Identify the blood parasite species.
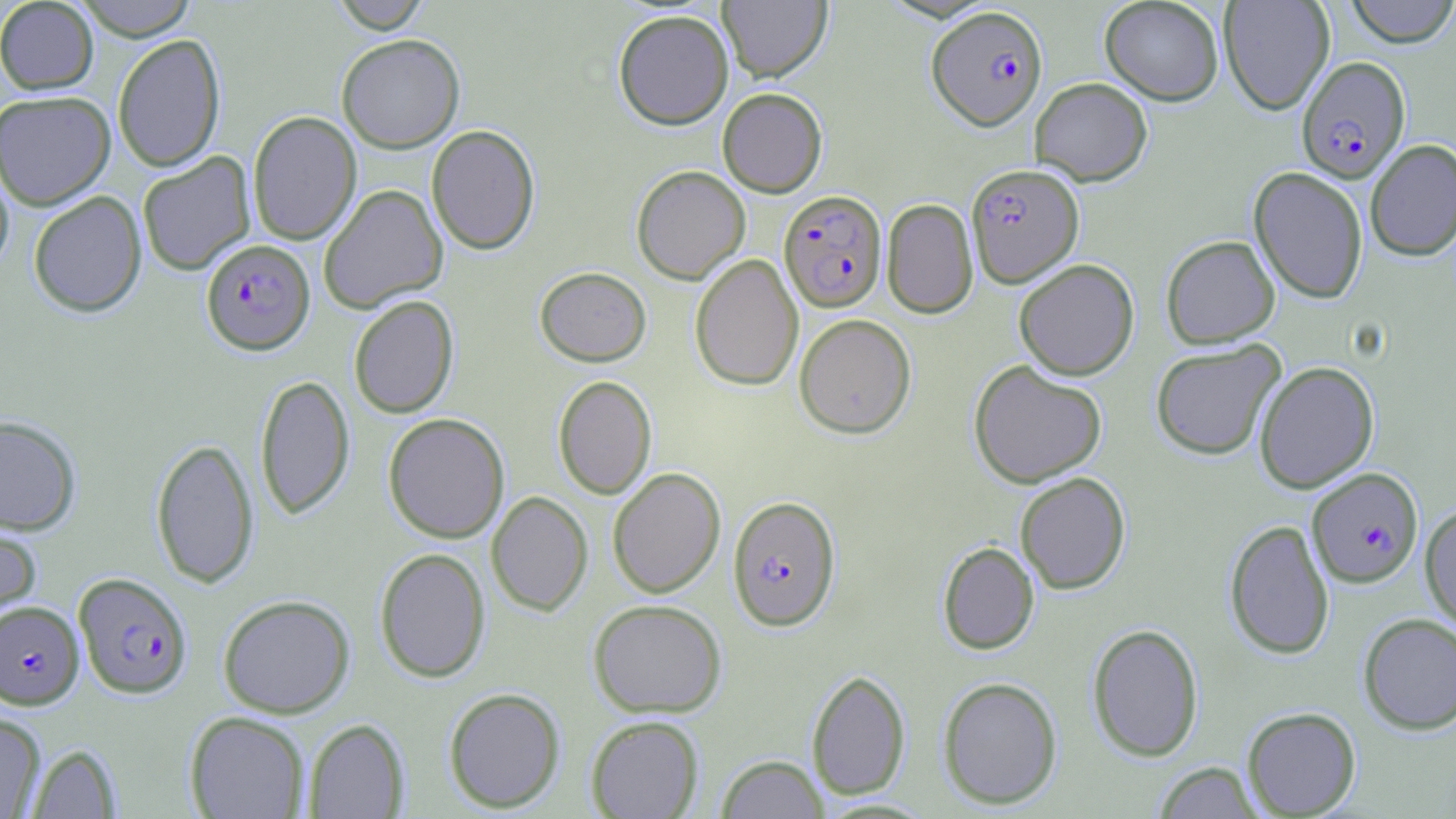

Plasmodium falciparum.

Summary:
  - Coordinate format: approximate bounding boxes as named x1/y1/x2/y2 corners in pixels
  - Plasmodium falciparum-infected red blood cell locations: (x1=927, y1=5, x2=1048, y2=130), (x1=1297, y1=56, x2=1411, y2=183), (x1=966, y1=163, x2=1084, y2=286), (x1=779, y1=189, x2=887, y2=312), (x1=201, y1=238, x2=315, y2=355), (x1=1307, y1=467, x2=1423, y2=587), (x1=727, y1=495, x2=841, y2=631), (x1=73, y1=572, x2=193, y2=698), (x1=1, y1=601, x2=84, y2=709)
  - Uninfected red blood cell locations: (x1=0, y1=0, x2=99, y2=94), (x1=72, y1=0, x2=198, y2=40), (x1=329, y1=0, x2=433, y2=33), (x1=718, y1=0, x2=832, y2=82), (x1=1099, y1=0, x2=1224, y2=105), (x1=1219, y1=0, x2=1334, y2=115), (x1=1343, y1=0, x2=1456, y2=47), (x1=613, y1=9, x2=733, y2=130), (x1=336, y1=33, x2=465, y2=153), (x1=112, y1=34, x2=226, y2=172), (x1=1029, y1=77, x2=1153, y2=186), (x1=717, y1=87, x2=827, y2=197), (x1=0, y1=90, x2=116, y2=209), (x1=247, y1=111, x2=362, y2=245), (x1=426, y1=124, x2=541, y2=255), (x1=1365, y1=139, x2=1456, y2=261), (x1=137, y1=152, x2=256, y2=276), (x1=0, y1=158, x2=14, y2=277), (x1=631, y1=165, x2=750, y2=284), (x1=1248, y1=166, x2=1368, y2=304), (x1=318, y1=184, x2=448, y2=313), (x1=28, y1=190, x2=147, y2=317), (x1=881, y1=199, x2=978, y2=318), (x1=1160, y1=235, x2=1280, y2=348), (x1=689, y1=254, x2=803, y2=391), (x1=1014, y1=259, x2=1139, y2=380), (x1=535, y1=266, x2=651, y2=366), (x1=348, y1=295, x2=459, y2=419), (x1=794, y1=313, x2=916, y2=438), (x1=1150, y1=340, x2=1286, y2=460), (x1=969, y1=360, x2=1107, y2=488), (x1=1254, y1=361, x2=1379, y2=493), (x1=254, y1=373, x2=355, y2=520), (x1=552, y1=375, x2=657, y2=500), (x1=383, y1=413, x2=510, y2=543), (x1=0, y1=414, x2=82, y2=535), (x1=150, y1=437, x2=259, y2=588), (x1=607, y1=467, x2=726, y2=598), (x1=1015, y1=472, x2=1131, y2=594), (x1=486, y1=491, x2=593, y2=616), (x1=1420, y1=503, x2=1456, y2=633), (x1=0, y1=517, x2=42, y2=629), (x1=1224, y1=519, x2=1334, y2=660), (x1=937, y1=541, x2=1039, y2=654), (x1=374, y1=547, x2=491, y2=683), (x1=217, y1=594, x2=355, y2=718), (x1=588, y1=599, x2=727, y2=718), (x1=1358, y1=612, x2=1456, y2=735), (x1=1086, y1=623, x2=1204, y2=762), (x1=806, y1=668, x2=911, y2=800), (x1=937, y1=676, x2=1063, y2=809), (x1=443, y1=687, x2=566, y2=813), (x1=1242, y1=706, x2=1361, y2=817), (x1=184, y1=711, x2=310, y2=819), (x1=0, y1=712, x2=46, y2=818), (x1=586, y1=715, x2=704, y2=818), (x1=304, y1=718, x2=410, y2=818), (x1=27, y1=743, x2=122, y2=818), (x1=716, y1=754, x2=829, y2=818), (x1=1153, y1=762, x2=1262, y2=818)
  - Magnification: 1000x
  - Image size: 1456×819 pixels
  - Modality: optical microscopy
  - Stain: May-Grünwald-Giemsa
  - Preparation: thin blood film
  - Field of view: single